Locate every blood parasite and identify its species.
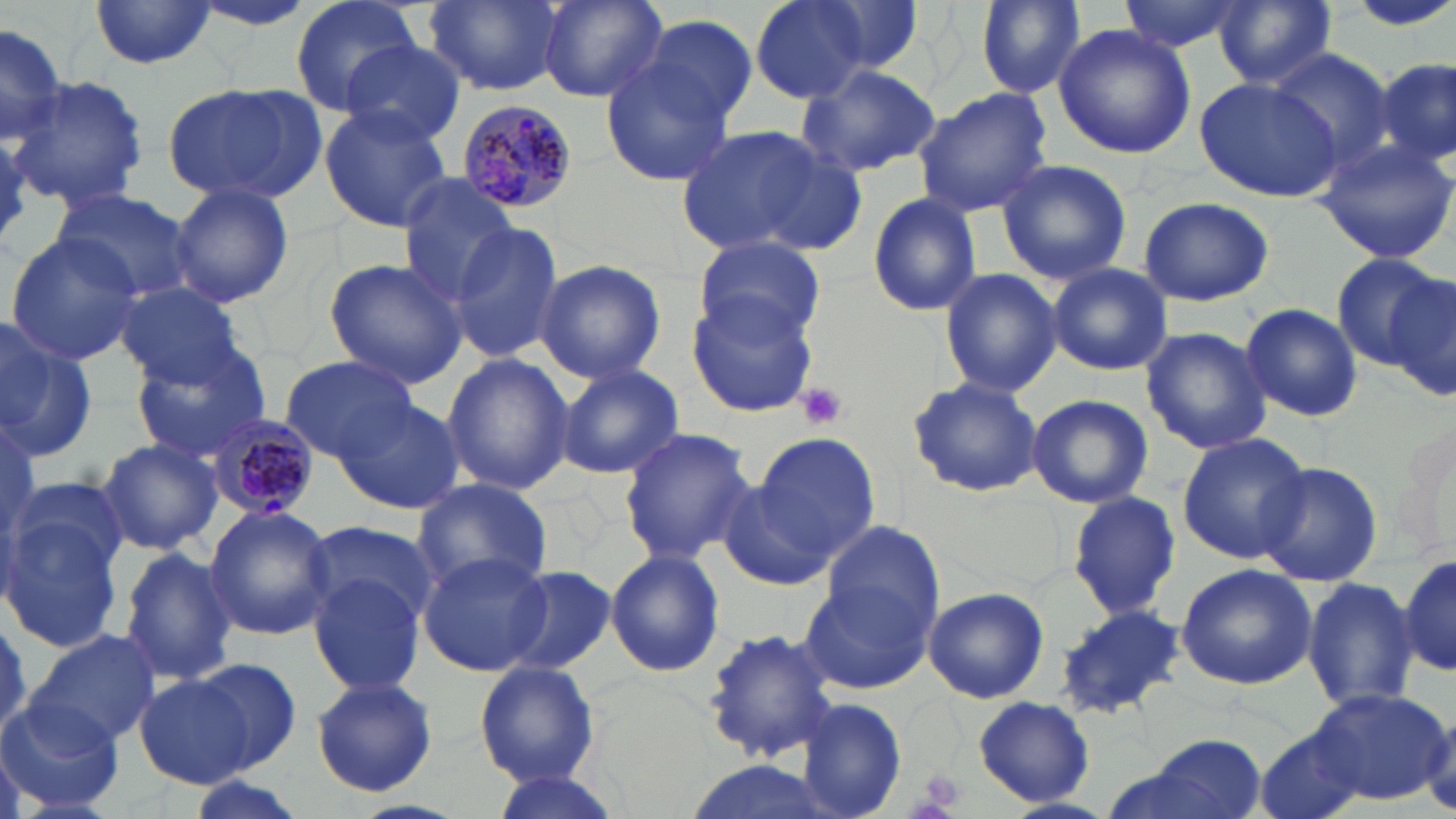

Approximate bounding boxes as named x1/y1/x2/y2 corners in pixels.
Plasmodium malariae-infected red blood cells: (x1=458, y1=99, x2=579, y2=216), (x1=207, y1=412, x2=323, y2=522).
No Plasmodium falciparum, Plasmodium ovale, Plasmodium vivax, Babesia divergens, or Trypanosoma brucei observed.

Platelet locations: (x1=795, y1=380, x2=850, y2=430), (x1=919, y1=768, x2=966, y2=810). Uninfected red blood cell locations: (x1=88, y1=0, x2=218, y2=70), (x1=290, y1=0, x2=421, y2=116), (x1=425, y1=0, x2=565, y2=94), (x1=539, y1=0, x2=667, y2=103), (x1=749, y1=0, x2=875, y2=103), (x1=813, y1=0, x2=927, y2=76), (x1=974, y1=0, x2=1084, y2=98), (x1=1117, y1=0, x2=1247, y2=53), (x1=1341, y1=0, x2=1456, y2=33), (x1=1211, y1=1, x2=1340, y2=89), (x1=639, y1=13, x2=759, y2=128), (x1=0, y1=20, x2=68, y2=150), (x1=1053, y1=24, x2=1195, y2=160), (x1=341, y1=41, x2=468, y2=148), (x1=1268, y1=51, x2=1397, y2=171), (x1=1376, y1=59, x2=1455, y2=169), (x1=601, y1=61, x2=735, y2=184), (x1=797, y1=62, x2=942, y2=180), (x1=8, y1=76, x2=150, y2=211), (x1=1195, y1=77, x2=1342, y2=202), (x1=161, y1=81, x2=326, y2=207), (x1=910, y1=87, x2=1054, y2=218), (x1=319, y1=105, x2=452, y2=234), (x1=676, y1=119, x2=851, y2=258), (x1=1313, y1=135, x2=1456, y2=266), (x1=996, y1=158, x2=1132, y2=283), (x1=395, y1=177, x2=522, y2=304), (x1=171, y1=184, x2=294, y2=308), (x1=51, y1=187, x2=198, y2=304), (x1=867, y1=193, x2=983, y2=317), (x1=1138, y1=196, x2=1274, y2=307), (x1=448, y1=224, x2=565, y2=362), (x1=4, y1=231, x2=145, y2=365), (x1=696, y1=233, x2=828, y2=346), (x1=1333, y1=254, x2=1445, y2=368), (x1=322, y1=258, x2=469, y2=390), (x1=535, y1=258, x2=666, y2=385), (x1=1048, y1=263, x2=1173, y2=375), (x1=939, y1=268, x2=1063, y2=398), (x1=1385, y1=269, x2=1456, y2=403), (x1=114, y1=282, x2=248, y2=387), (x1=686, y1=293, x2=817, y2=416), (x1=1240, y1=303, x2=1364, y2=422), (x1=0, y1=318, x2=97, y2=462), (x1=1140, y1=326, x2=1273, y2=454), (x1=127, y1=339, x2=272, y2=462), (x1=441, y1=352, x2=573, y2=495), (x1=279, y1=355, x2=421, y2=462), (x1=552, y1=362, x2=684, y2=480), (x1=908, y1=375, x2=1043, y2=497), (x1=1024, y1=394, x2=1155, y2=510), (x1=335, y1=396, x2=464, y2=514), (x1=0, y1=409, x2=41, y2=556), (x1=1397, y1=424, x2=1454, y2=546), (x1=617, y1=427, x2=755, y2=565), (x1=751, y1=432, x2=881, y2=566), (x1=1176, y1=432, x2=1312, y2=564), (x1=96, y1=437, x2=222, y2=556), (x1=1255, y1=460, x2=1384, y2=588), (x1=718, y1=478, x2=836, y2=589), (x1=408, y1=479, x2=553, y2=600), (x1=1066, y1=490, x2=1180, y2=619), (x1=202, y1=504, x2=337, y2=643), (x1=0, y1=507, x2=128, y2=653), (x1=819, y1=517, x2=947, y2=636), (x1=301, y1=518, x2=441, y2=633), (x1=116, y1=546, x2=235, y2=686), (x1=605, y1=549, x2=725, y2=678), (x1=1399, y1=549, x2=1455, y2=680), (x1=416, y1=550, x2=553, y2=677), (x1=1175, y1=564, x2=1318, y2=688), (x1=499, y1=566, x2=616, y2=676), (x1=307, y1=573, x2=427, y2=698), (x1=801, y1=576, x2=936, y2=693), (x1=1301, y1=576, x2=1419, y2=714), (x1=923, y1=586, x2=1049, y2=704), (x1=1054, y1=604, x2=1187, y2=721), (x1=0, y1=613, x2=35, y2=736), (x1=700, y1=624, x2=841, y2=764), (x1=29, y1=627, x2=158, y2=748), (x1=186, y1=655, x2=306, y2=774), (x1=474, y1=660, x2=602, y2=787), (x1=135, y1=675, x2=256, y2=789), (x1=310, y1=676, x2=439, y2=797), (x1=1308, y1=689, x2=1450, y2=806), (x1=971, y1=696, x2=1094, y2=806), (x1=0, y1=697, x2=121, y2=813), (x1=798, y1=698, x2=908, y2=819), (x1=1257, y1=730, x2=1366, y2=819), (x1=1116, y1=737, x2=1270, y2=819), (x1=486, y1=771, x2=623, y2=819), (x1=182, y1=776, x2=304, y2=819). Slide-level diagnosis: Plasmodium malariae. Light microscopy. Single field of view. Thin blood film. 1000x magnification. May-Grünwald-Giemsa-stained preparation. Image is 1456×819 pixels.